Identify the parasite.
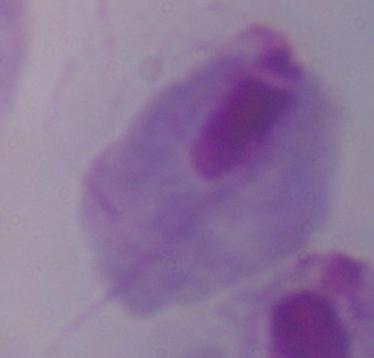

This is a trichomonad.

Photomicrograph. 1000x magnification.